Assess this cell for malaria.
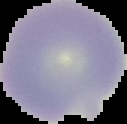
It is uninfected.

Segmented cell region on a black background. From a thin blood film. Image is 127×124 pixels.